Give the position of every Plasmodium parasite and every leukocyte.
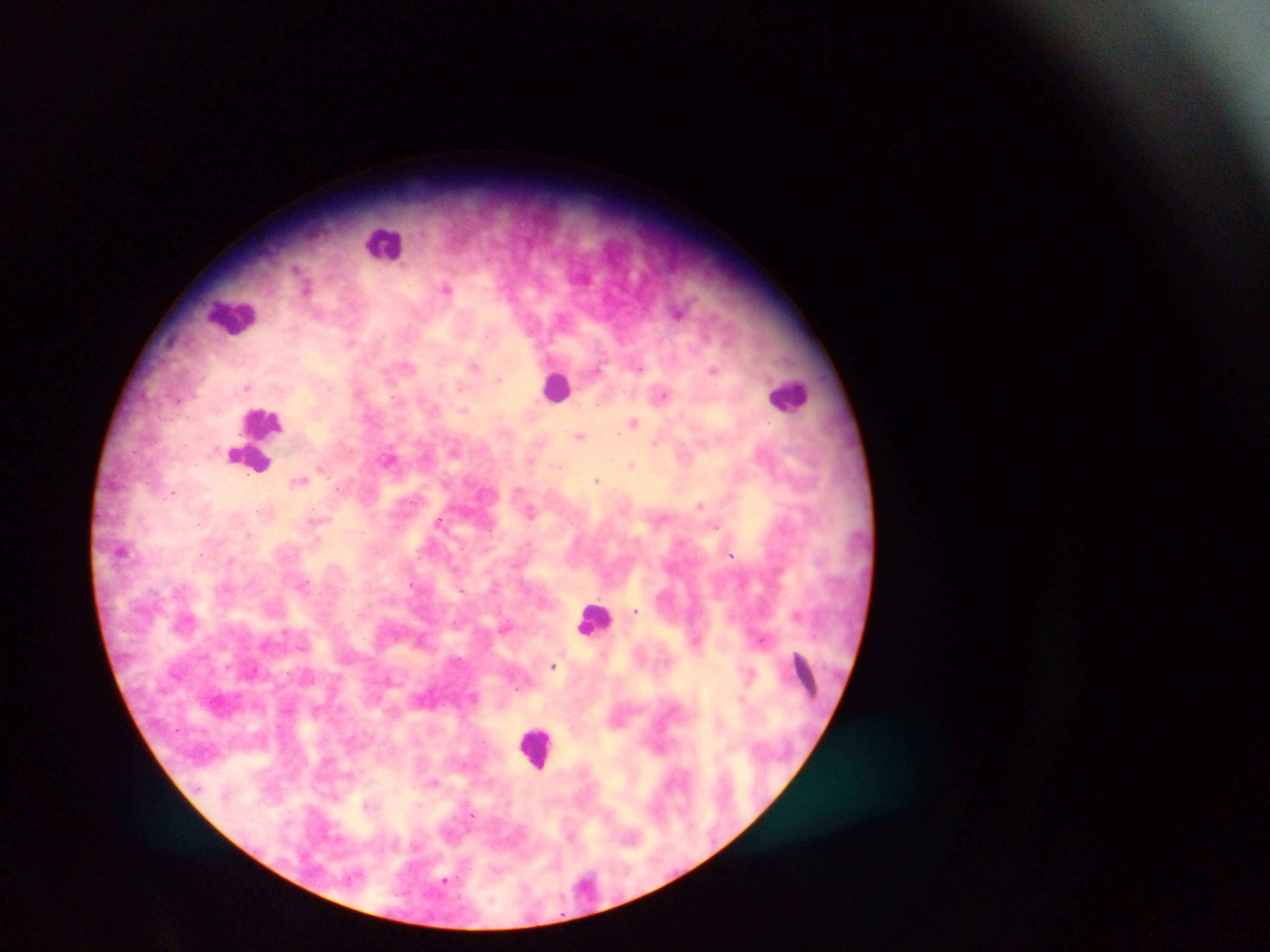

Approximate centers as [x, y] in pixels.
Plasmodium parasites: [448, 289], [679, 312], [475, 366], [714, 369], [247, 385], [662, 395], [465, 409], [633, 422], [580, 435], [655, 442], [391, 459], [632, 465], [321, 467], [299, 480], [597, 480], [173, 491], [700, 504], [531, 511], [316, 520], [439, 520], [732, 554], [304, 583], [411, 583], [636, 610], [798, 614], [507, 627], [761, 638], [553, 665], [750, 673], [475, 697], [434, 782], [445, 881].
Leukocytes: [385, 243], [234, 315], [557, 386], [789, 394], [254, 439], [594, 619], [807, 678], [538, 747].

image size = 1270×952 pixels
field of view = single
capture = mobile-phone photograph through a microscope
preparation = thick blood smear
country = Ghana